Give the position of every leukocyte visible.
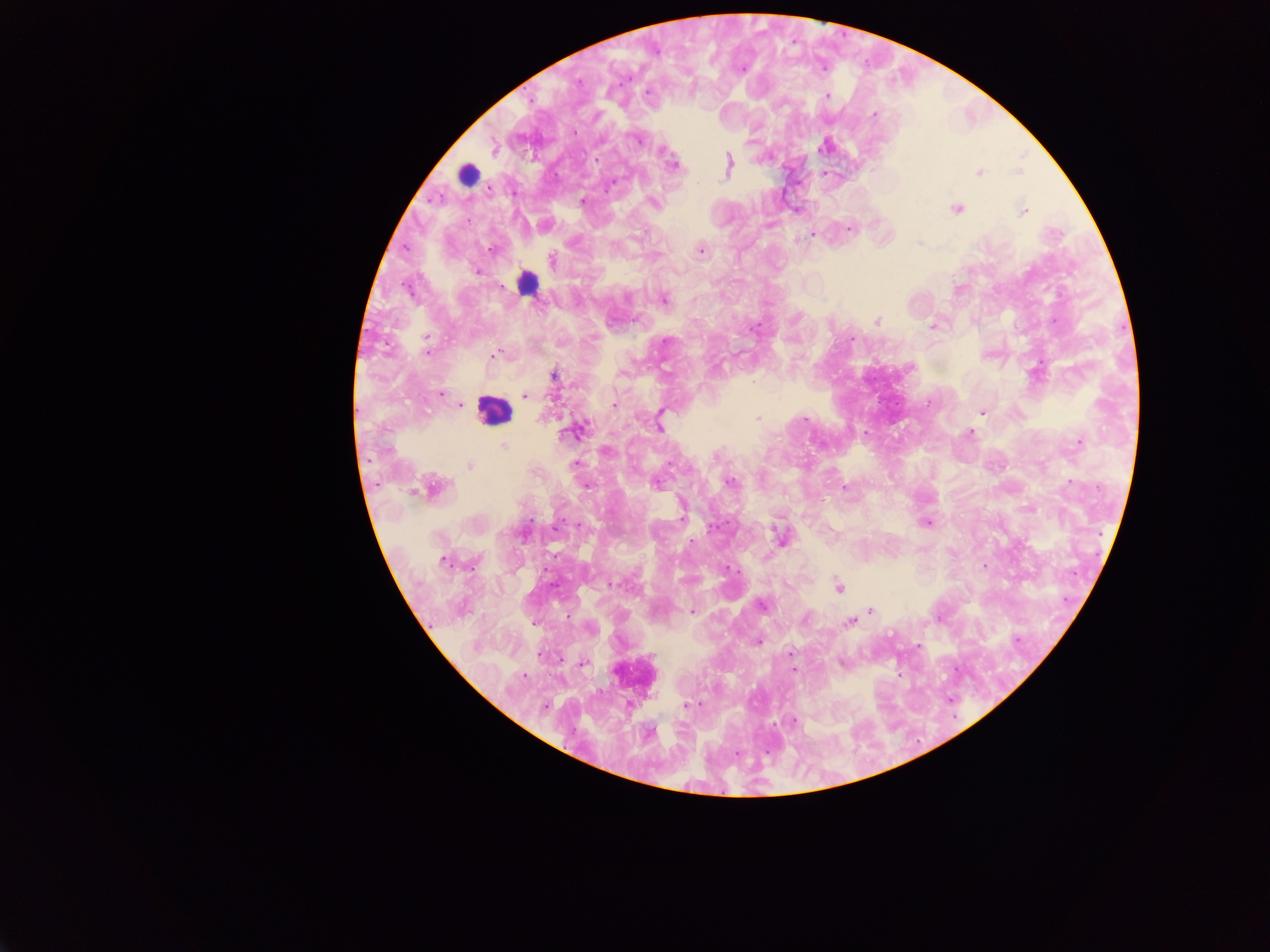
Approximate centers as {x, y} in pixels.
Leukocytes: {467, 174}, {526, 282}, {493, 410}, {633, 674}.

Summary:
  - Malaria parasite locations: {741, 68}, {577, 81}, {647, 92}, {827, 96}, {874, 114}, {637, 137}, {493, 146}, {824, 146}, {663, 150}, {673, 164}, {728, 165}, {1018, 171}, {978, 172}, {825, 173}, {582, 201}, {652, 202}, {796, 209}, {956, 209}, {1022, 211}, {849, 228}, {813, 234}, {798, 241}, {492, 249}, {700, 250}, {551, 260}, {477, 270}, {663, 299}, {877, 320}, {933, 326}, {852, 337}, {426, 338}, {493, 355}, {553, 375}, {441, 393}, {525, 395}, {459, 404}, {615, 406}, {982, 411}, {758, 418}, {805, 418}, {659, 426}, {574, 431}, {970, 433}, {1079, 442}, {505, 449}, {605, 451}, {469, 465}, {575, 465}, {729, 482}, {657, 483}, {586, 484}, {431, 488}, {844, 488}, {927, 522}, {523, 532}, {781, 538}, {443, 560}, {983, 566}, {839, 588}, {762, 604}, {870, 610}, {693, 612}, {805, 618}, {850, 621}, {534, 623}, {589, 628}, {758, 642}, {917, 646}, {790, 654}, {583, 662}, {841, 663}, {793, 671}, {688, 706}, {792, 721}
  - Preparation: thick blood smear
  - Capture: mobile-phone photograph through a microscope
  - Field of view: single
  - Image size: 1270×952 pixels
  - Country: Ghana